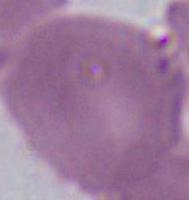
{
  "identification": "red blood cell",
  "modality": "micrograph",
  "magnification": "1000x"
}